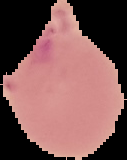
Summary:
  - Image type: segmented cell region on a black background
  - Result: no malaria parasites detected
  - Preparation: thin blood film
  - Image size: 127×160 pixels